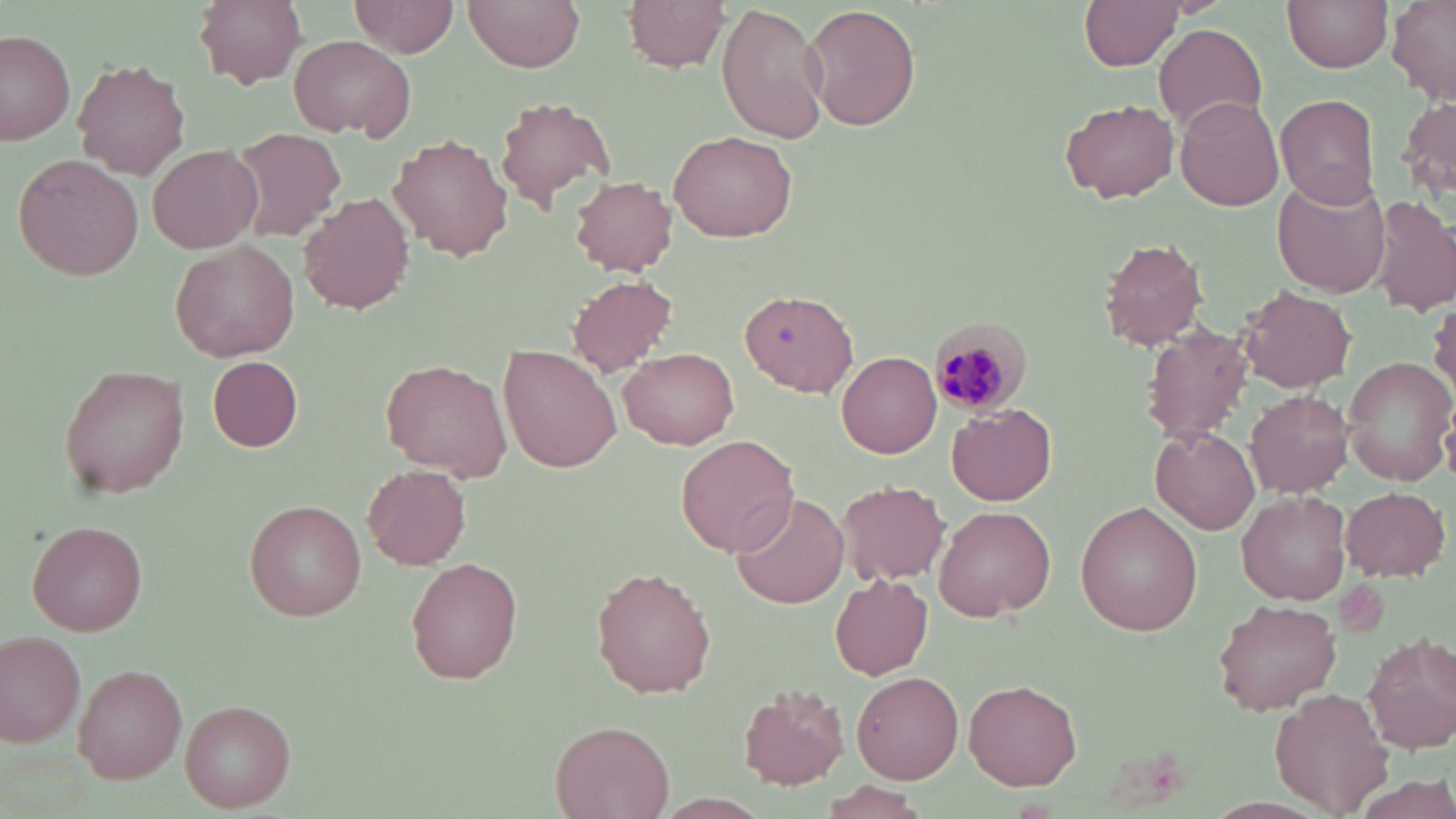

Plasmodium malariae-infected red blood cell locations = approximate bounding boxes as (x1, y1, x2, y2) in pixels: (925, 317, 1031, 416)
slide-level diagnosis = Plasmodium malariae
image size = 1456×819 pixels
uninfected red blood cell locations = approximate bounding boxes as (x1, y1, x2, y2) in pixels: (194, 0, 308, 88), (351, 0, 459, 57), (465, 0, 583, 72), (625, 0, 731, 71), (1283, 0, 1395, 73), (1081, 1, 1188, 70), (716, 3, 830, 143), (1386, 3, 1455, 106), (804, 5, 919, 133), (1156, 26, 1265, 128), (0, 30, 75, 146), (290, 35, 414, 138), (73, 60, 191, 179), (1274, 93, 1380, 208), (1176, 95, 1284, 213), (492, 96, 615, 212), (1404, 98, 1455, 202), (1061, 101, 1178, 201), (226, 126, 346, 243), (669, 130, 798, 242), (390, 135, 511, 260), (149, 144, 262, 253), (13, 154, 144, 281), (570, 176, 678, 275), (1273, 178, 1392, 296), (298, 192, 413, 315), (1370, 196, 1456, 314), (1099, 237, 1209, 351), (171, 239, 299, 364), (567, 274, 676, 376), (1239, 286, 1357, 394), (740, 290, 856, 396), (1429, 299, 1456, 399), (1139, 322, 1256, 447), (499, 345, 621, 474), (620, 348, 740, 450), (836, 350, 941, 458), (1343, 356, 1454, 486), (208, 357, 302, 451), (383, 357, 511, 479), (57, 364, 189, 501), (1245, 390, 1354, 496), (948, 403, 1057, 506), (1151, 425, 1261, 534), (677, 431, 800, 558), (362, 466, 471, 570), (838, 479, 950, 585), (1341, 486, 1451, 580), (731, 492, 850, 609), (1239, 492, 1351, 605), (246, 500, 366, 621), (1076, 501, 1203, 635), (933, 507, 1056, 619), (27, 521, 147, 636), (408, 558, 524, 683), (593, 566, 717, 698), (830, 572, 934, 678), (1213, 598, 1342, 715), (0, 630, 87, 747), (1363, 631, 1456, 752), (74, 664, 187, 783), (851, 670, 964, 784), (964, 680, 1081, 790), (737, 684, 849, 791), (1270, 689, 1392, 814), (181, 700, 296, 811), (552, 720, 675, 817), (1358, 775, 1455, 817), (817, 782, 932, 819), (649, 794, 776, 818)
stain = May-Grünwald-Giemsa
preparation = thin blood smear
modality = light microscopy
field of view = single
magnification = 1000x